Describe the morphology of the erythrocytes.
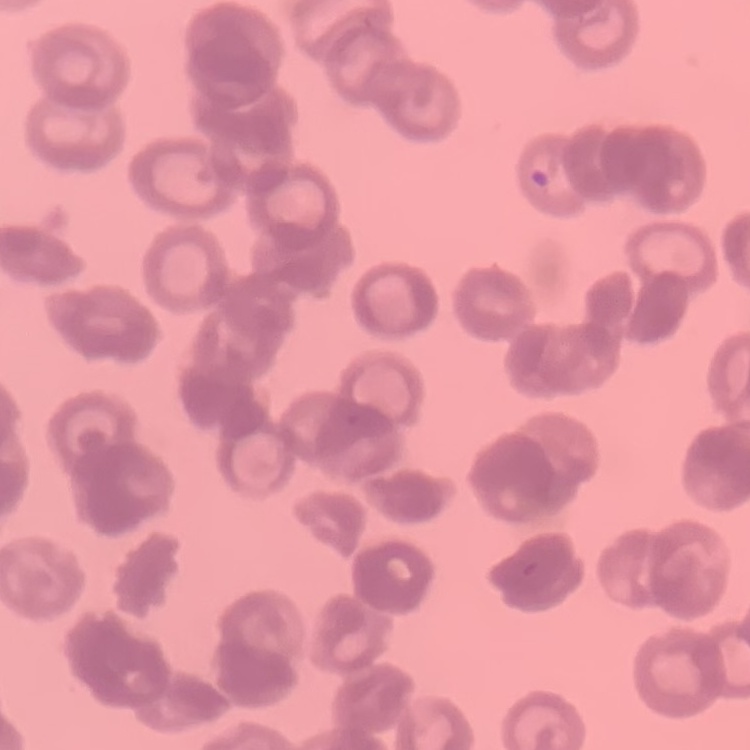

They show rouleaux formation.

Summary:
  - Stain: Field's or Giemsa
  - Preparation: thin blood smear
  - Image type: one tile cut from a larger photomicrograph